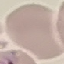
Malaria status: uninfected. Thin blood smear. Giemsa-stained preparation. Cell patch, automatically extracted from a larger field of view and resized to 64 × 64 pixels. Acquired by smartphone through the microscope eyepiece.